Classify this cell by malaria status.
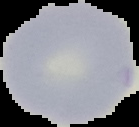

Uninfected.

Cell region segmented out of the field of view; the surrounding area is masked to black. Image is 139×127 pixels. From a thin blood smear.